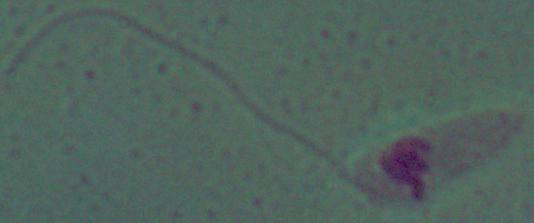

{
  "modality": "micrograph",
  "identification": "Leishmania",
  "magnification": "1000x"
}